Assess the morphology of the red blood cells.
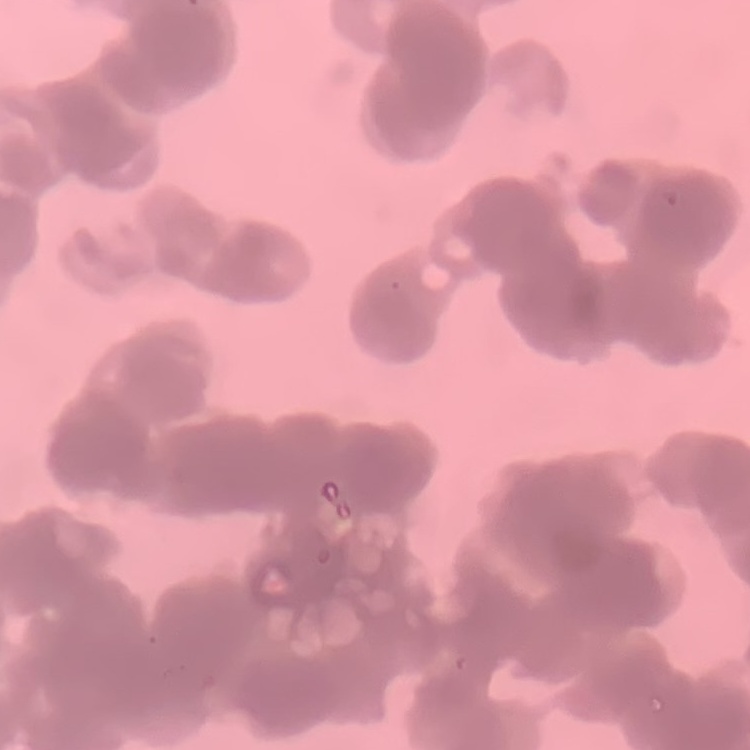

They show rouleaux formation.

{
  "stain": "Field's or Giemsa",
  "preparation": "thin blood smear",
  "image_type": "square crop of a larger photomicrograph"
}